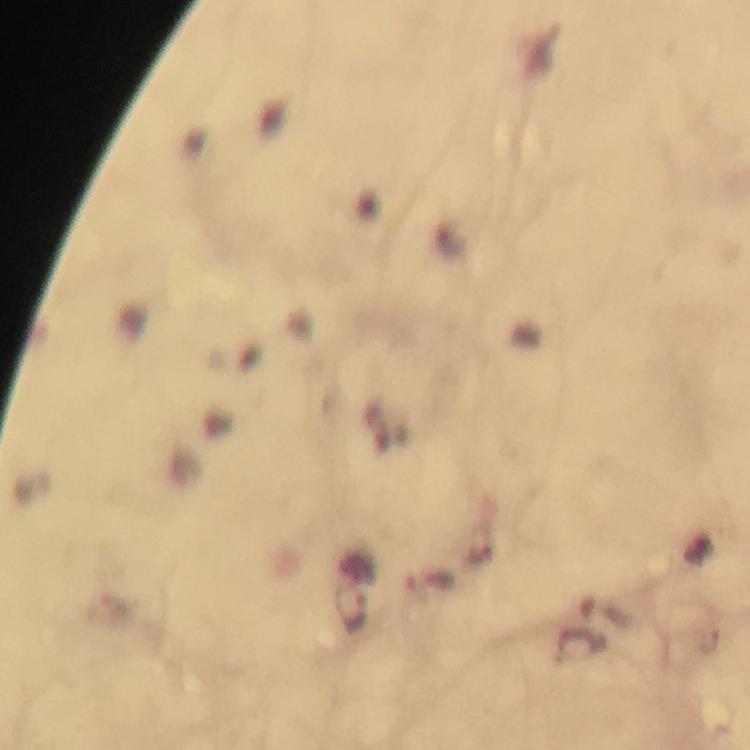
Approximate object centers, in pixels from the top-left corner.
Summary:
  - Plasmodium parasite locations: (x=350, y=609)
  - Magnification: 100x
  - Cropped from: a single field of view
  - Preparation: thick blood film
  - Image size: 750×750 pixels
  - Capture: smartphone camera through the microscope
  - Context: from a malaria diagnostic workup
  - Immersion oil: used
  - Stain: Giemsa